Comment on the morphology of the red blood cells.
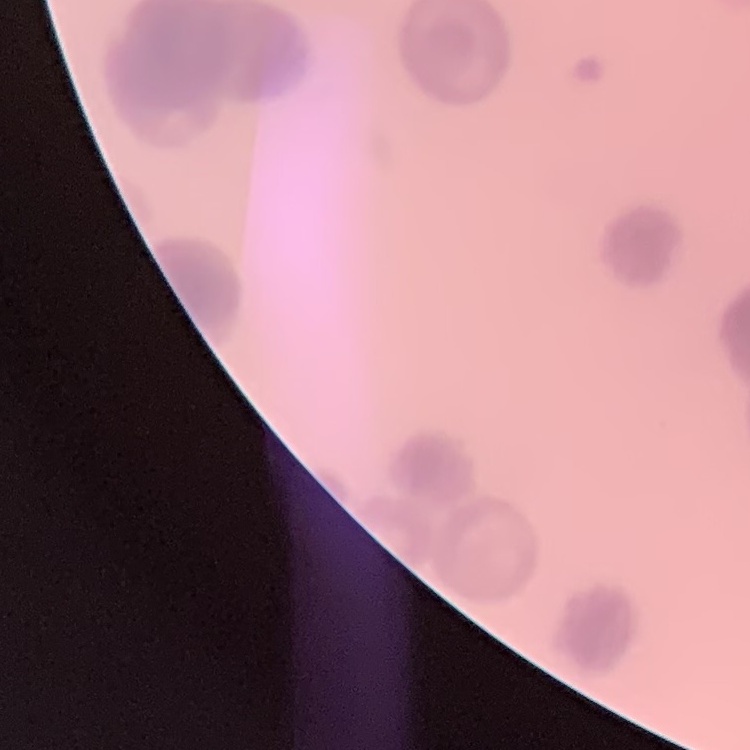
Rouleaux formation.

preparation = thin blood film
image type = square crop of a larger photomicrograph
stain = Field's or Giemsa